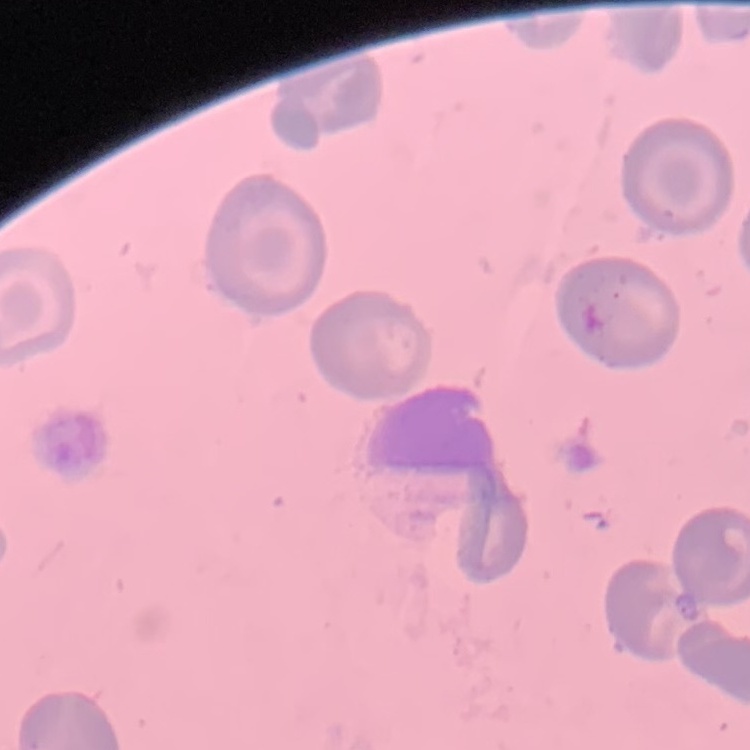
Summary:
  - Red blood cell morphology: no rouleaux formation
  - Stain: Field's or Giemsa
  - Image type: one tile cut from a larger photomicrograph
  - Preparation: thin peripheral smear